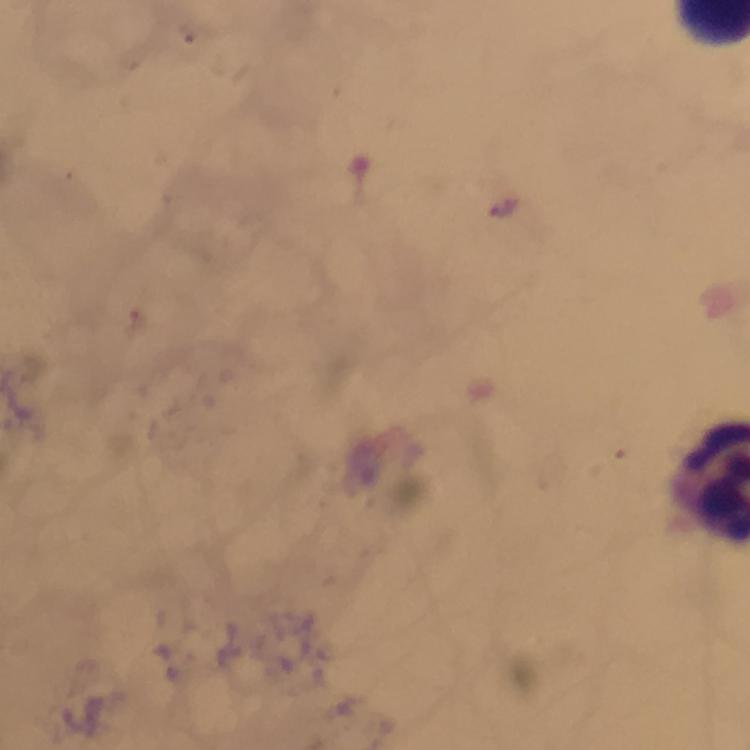

Approximate centers as [x, y] in pixels.
Summary:
  - Plasmodium parasite locations: [504, 206]
  - Preparation: thick blood film
  - Context: from a diagnostic examination for malaria
  - Stain: Giemsa
  - Cropped from: one field of view
  - Capture: smartphone photograph through a microscope
  - Immersion oil: used
  - Magnification: 100x
  - Image size: 750×750 pixels